Identify the blood parasite species.
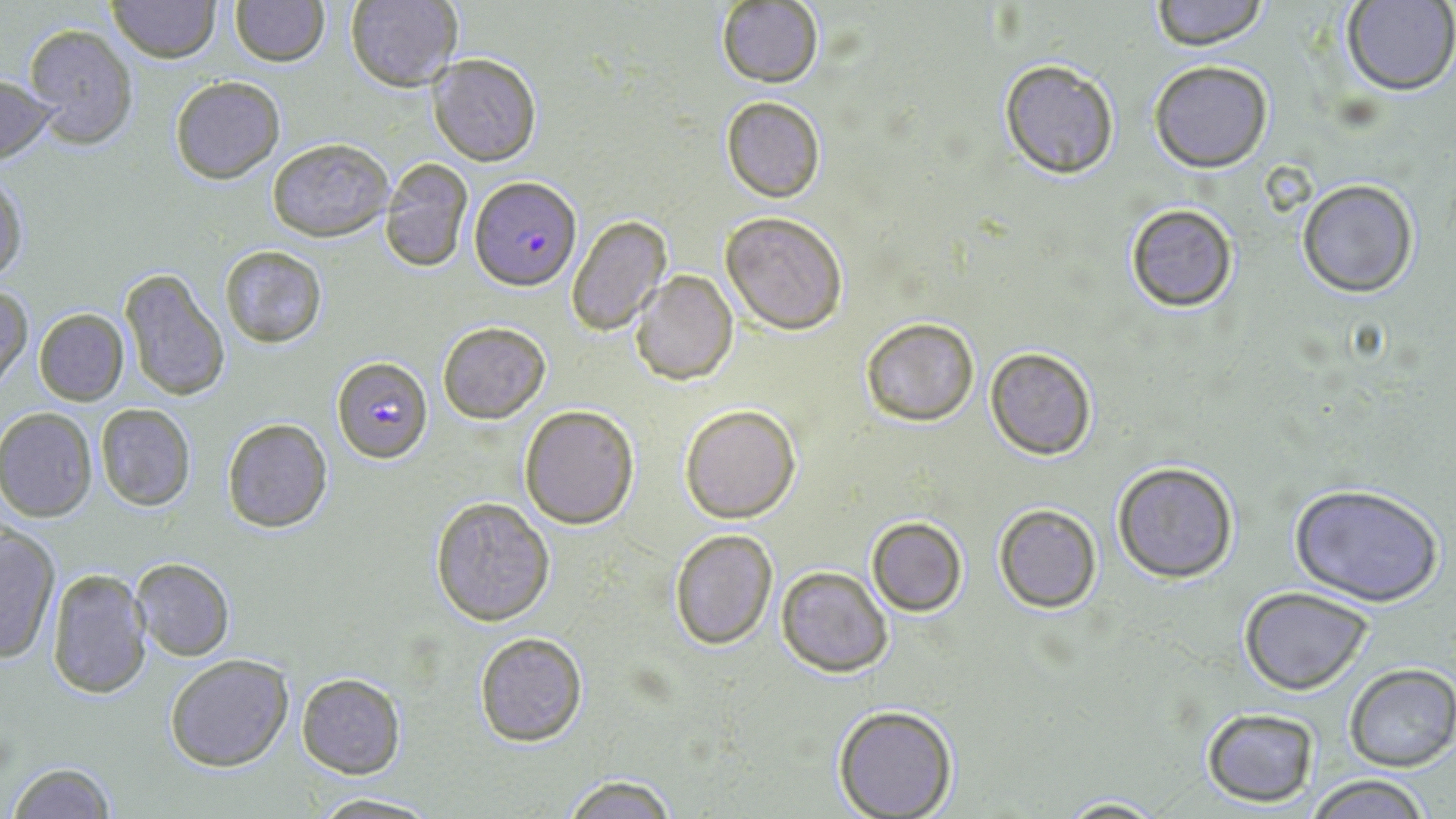
Plasmodium falciparum.

Summary:
  - Coordinate format: approximate bounding boxes as (x1,y1)-(x2,y2) corner pairs in pixels
  - Plasmodium falciparum-infected red blood cell locations: (471,176)-(580,291), (334,354)-(430,464)
  - Uninfected red blood cell locations: (107,0)-(219,62), (228,0)-(328,66), (344,0)-(463,90), (1147,0)-(1271,50), (717,1)-(824,88), (1342,1)-(1456,95), (21,23)-(138,148), (429,54)-(541,165), (998,58)-(1120,180), (1149,59)-(1273,171), (0,74)-(57,163), (170,76)-(284,183), (721,96)-(825,202), (267,138)-(394,242), (380,158)-(474,273), (0,173)-(27,285), (1297,178)-(1419,298), (1124,202)-(1240,312), (721,210)-(849,335), (566,214)-(672,336), (218,245)-(328,348), (117,266)-(230,402), (630,272)-(738,386), (0,282)-(32,385), (33,308)-(129,405), (859,317)-(981,425), (437,321)-(551,423), (985,347)-(1099,460), (95,403)-(196,512), (679,403)-(801,522), (518,404)-(639,529), (0,407)-(97,521), (221,418)-(334,533), (1112,460)-(1240,584), (1288,484)-(1444,608), (429,496)-(556,626), (993,504)-(1102,613), (866,515)-(968,617), (0,526)-(61,664), (667,527)-(778,649), (131,557)-(234,660), (774,565)-(893,678), (45,568)-(150,697), (1239,586)-(1375,696), (474,632)-(588,747), (164,654)-(294,772), (1344,664)-(1456,772), (295,673)-(406,777), (832,705)-(958,819), (1200,707)-(1320,807), (3,761)-(118,818), (1301,774)-(1437,818), (557,775)-(684,818), (305,793)-(442,818), (1053,795)-(1169,817)
  - Stain: May-Grünwald-Giemsa
  - Modality: optical microscopy
  - Image size: 1456×819 pixels
  - Magnification: 1000x
  - Field of view: one of a larger specimen
  - Preparation: thin blood film